Give the position of every Plasmodium parasite visible.
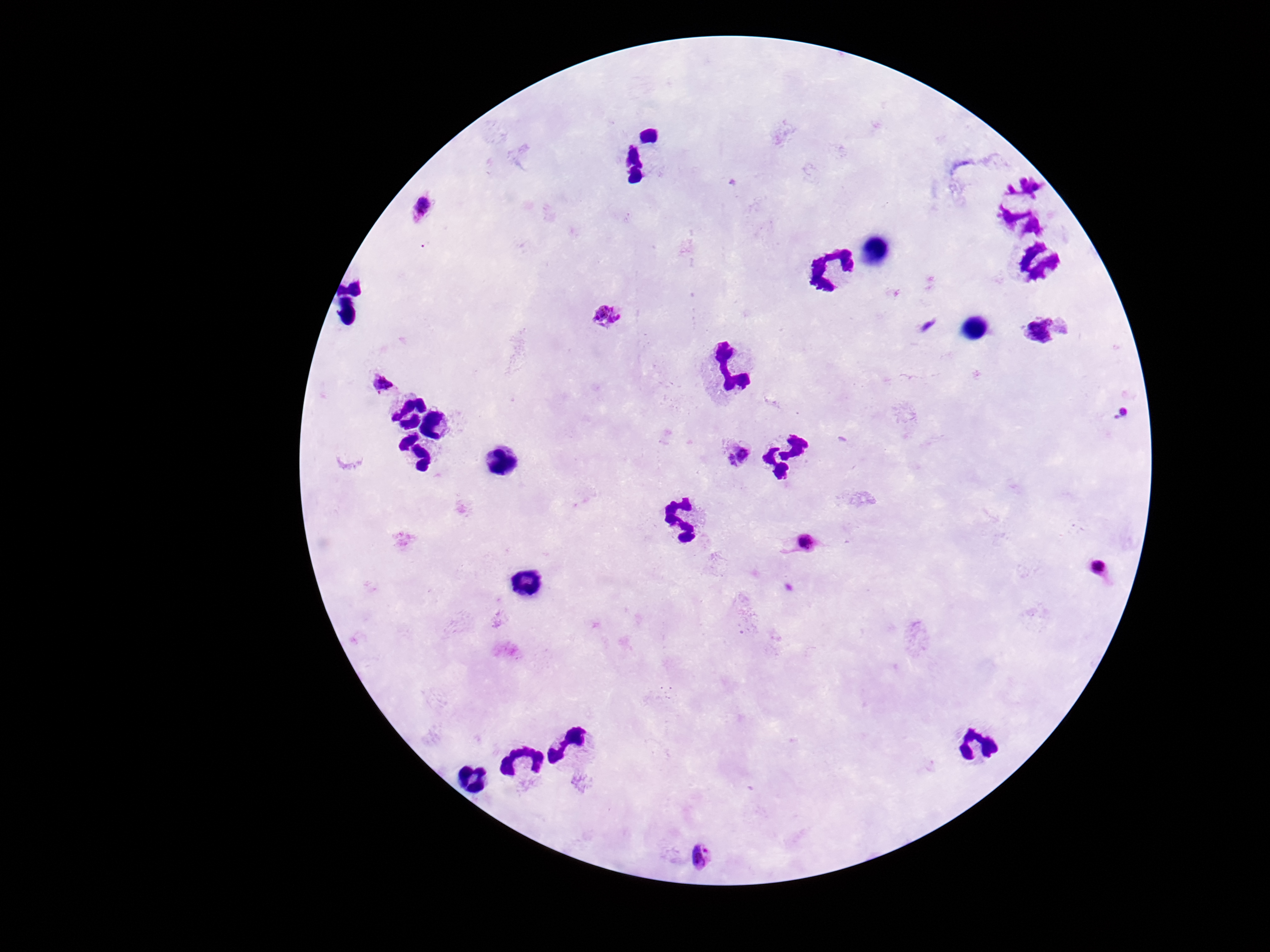

Approximate object centers, in pixels from the top-left corner.
Plasmodium parasites: (x=423, y=208), (x=606, y=316), (x=1044, y=331), (x=381, y=383), (x=1122, y=413), (x=739, y=455), (x=806, y=544), (x=1099, y=568), (x=702, y=855).

100x magnification. Patient malaria status: positive. Giemsa stain. Smartphone photograph taken through the microscope eyepiece. Image is 1270×952 pixels. One field from this slide. Thick blood film.